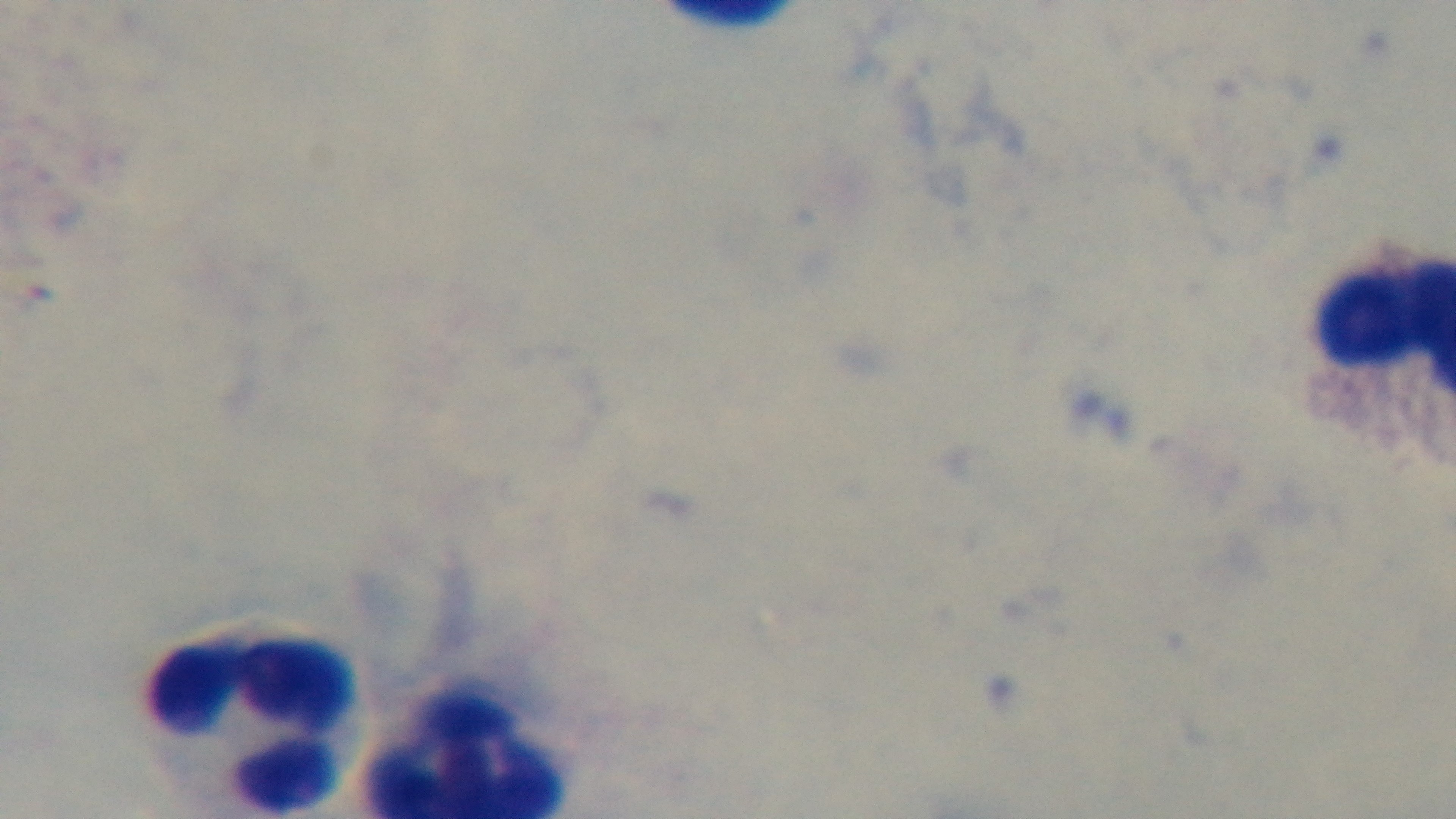
preparation = thick
field of view = one from the slide
capture = mounted 4K digital camera
malaria status = uninfected
objective = 100x oil immersion
stain = Giemsa
modality = light microscopy